Assess this cell for malaria.
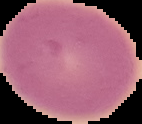
Uninfected.

Summary:
  - Image type: cell region segmented out of the field of view; surrounding area masked to black
  - Preparation: thin blood film
  - Image size: 142×124 pixels